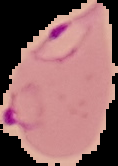

{
  "image_type": "cell region segmented out of the field of view; surrounding area masked to black",
  "image_size": "118×166 pixels",
  "preparation": "thin blood film",
  "result": "Plasmodium parasites identified"
}